Identify the blood parasite species.
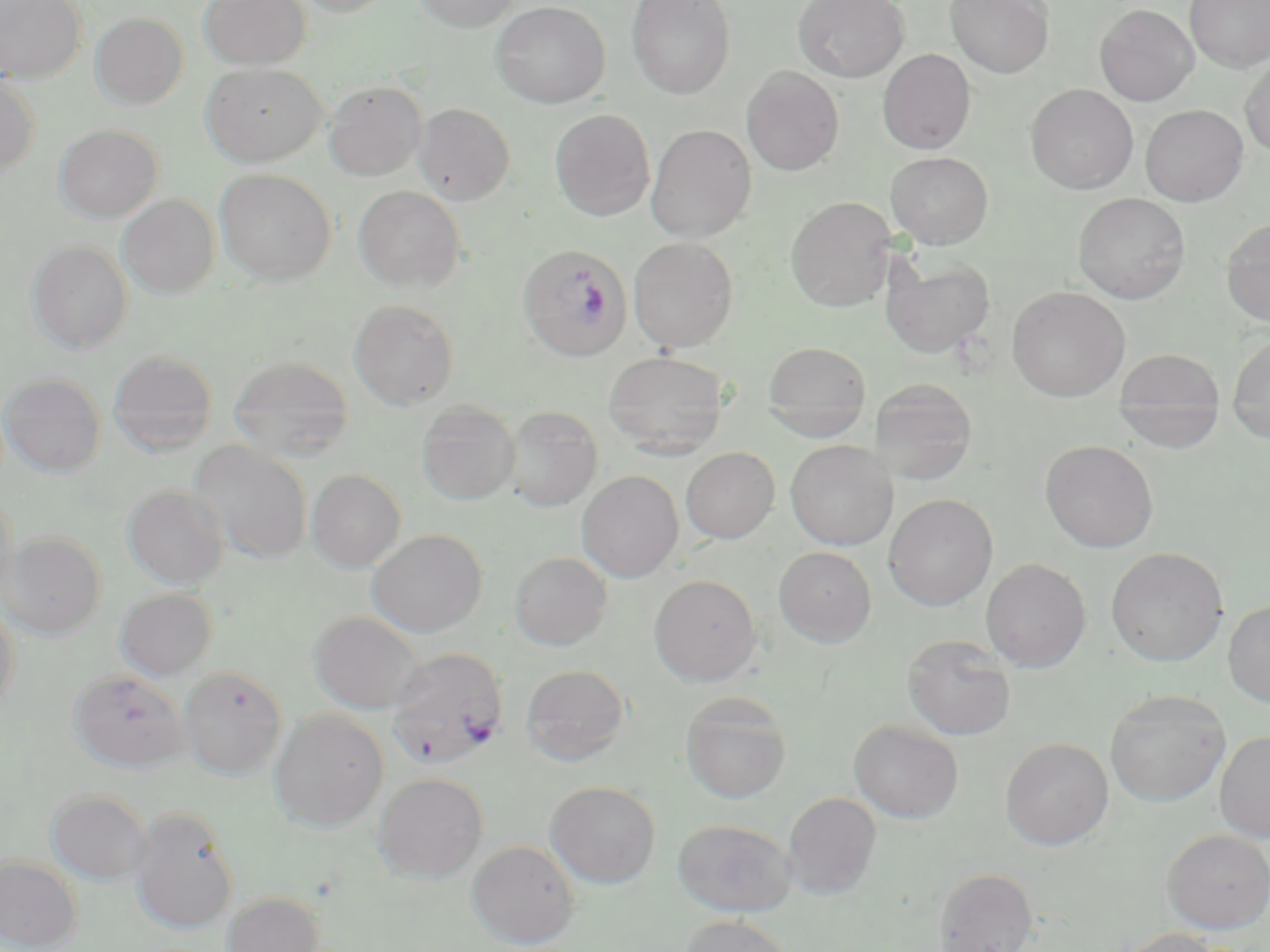
Plasmodium falciparum.

Approximate bounding boxes as (x1,y1)-(x2,y2) corner pairs in pixels. Uninfected red blood cell locations: (0,0)-(86,83), (199,0)-(310,70), (295,0)-(397,17), (412,0)-(521,32), (625,0)-(736,99), (793,0)-(909,82), (945,0)-(1054,78), (1185,0)-(1270,72), (490,2)-(609,107), (1094,3)-(1199,106), (0,4)-(187,96), (90,12)-(188,109), (877,49)-(976,154), (1240,54)-(1270,158), (201,62)-(327,166), (741,66)-(844,176), (0,76)-(40,178), (322,80)-(427,181), (1025,84)-(1138,194), (413,103)-(515,205), (1140,104)-(1248,206), (550,109)-(655,221), (54,123)-(162,222), (645,124)-(756,242), (885,151)-(993,248), (214,168)-(336,286), (353,186)-(465,291), (1073,192)-(1191,304), (117,195)-(219,298), (785,196)-(896,312), (1221,217)-(1270,327), (628,237)-(739,352), (26,240)-(133,354), (881,254)-(995,358), (1007,286)-(1130,402), (348,298)-(459,410), (1227,333)-(1270,444), (762,341)-(872,441), (107,349)-(218,456), (1113,349)-(1226,451), (603,351)-(729,459), (228,356)-(355,462), (1,372)-(105,476), (869,378)-(978,484), (416,401)-(520,505), (502,406)-(603,512), (1040,439)-(1158,552), (188,440)-(312,564), (785,440)-(898,550), (680,447)-(780,543), (307,469)-(406,572), (577,471)-(684,582), (123,485)-(228,589), (0,486)-(18,600), (883,493)-(998,610), (368,529)-(487,637), (1,531)-(106,639), (773,546)-(877,646), (1106,546)-(1228,667), (509,551)-(613,651), (980,558)-(1091,672), (649,574)-(761,685), (114,588)-(218,680), (1223,599)-(1270,707), (0,601)-(20,716), (308,611)-(425,714), (903,633)-(1016,740), (521,664)-(631,765), (178,666)-(287,779), (69,669)-(190,772), (1105,689)-(1230,806), (680,693)-(792,803), (269,710)-(389,832), (849,719)-(964,823), (1215,730)-(1270,843), (1001,737)-(1114,849), (373,772)-(489,883), (546,781)-(661,888), (45,789)-(152,885), (783,792)-(881,899), (129,807)-(238,934), (673,819)-(796,916), (1161,828)-(1270,933), (467,839)-(580,948), (0,855)-(83,952), (933,867)-(1038,952), (221,891)-(325,952), (677,915)-(796,952), (1115,927)-(1227,952). Plasmodium falciparum-infected red blood cell locations: (518,243)-(631,362), (387,647)-(509,769). Image is 1270×952 pixels. Light microscopy. Thin blood film. Single field of view. May-Grünwald-Giemsa stain. 1000x magnification.